Give the preparation type.
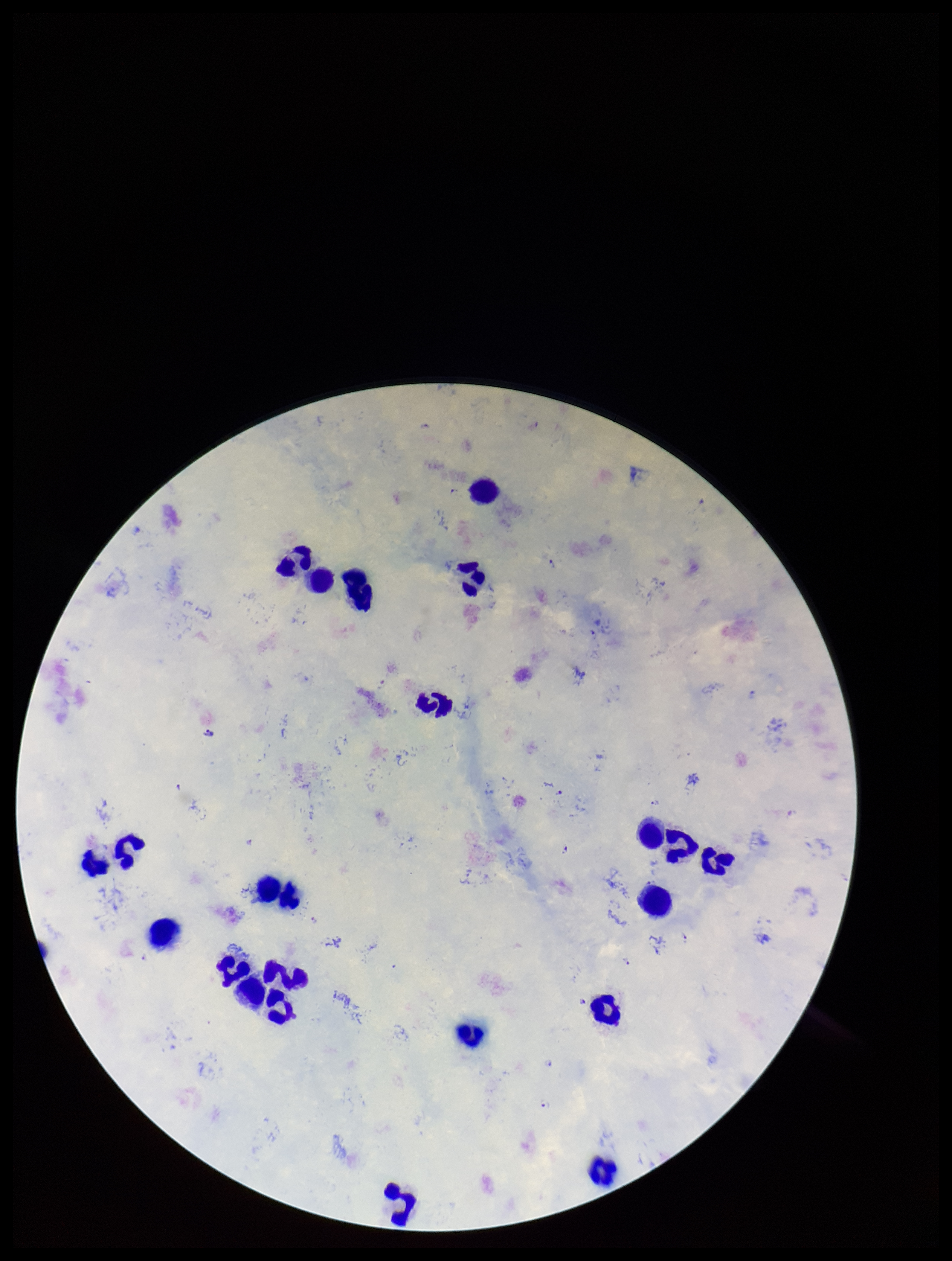
Thick.

parasite_count: 5
leukocyte_count: 23
patient_malaria_status: positive
capture: smartphone photograph through the microscope eyepiece
image_size: 952×1261 pixels
plasmodium_parasites: detected
stain: Giemsa
field_of_view: one from this slide
species_reported_for_this_patient: Plasmodium falciparum